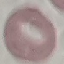
result = negative for malaria parasites
capture = smartphone through the microscope eyepiece
preparation = thin blood smear
stain = Giemsa
image type = automatically extracted cell patch, resized to 64 × 64 pixels